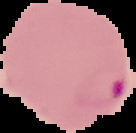

From a thin blood smear. Result: Plasmodium parasites detected. Image is 136×133 pixels. Segmented cell region on a black background.